State which parasite is depicted.
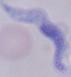

A trypanosome.

Summary:
  - Modality: micrograph
  - Magnification: 1000x